Classify this cell by malaria status.
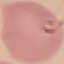

Parasitized.

Summary:
  - Stain: Giemsa
  - Image type: cell patch, automatically extracted from a larger field of view and resized to 64 × 64 pixels
  - Capture: smartphone camera at the microscope eyepiece
  - Preparation: thin smear